State the blood parasite species.
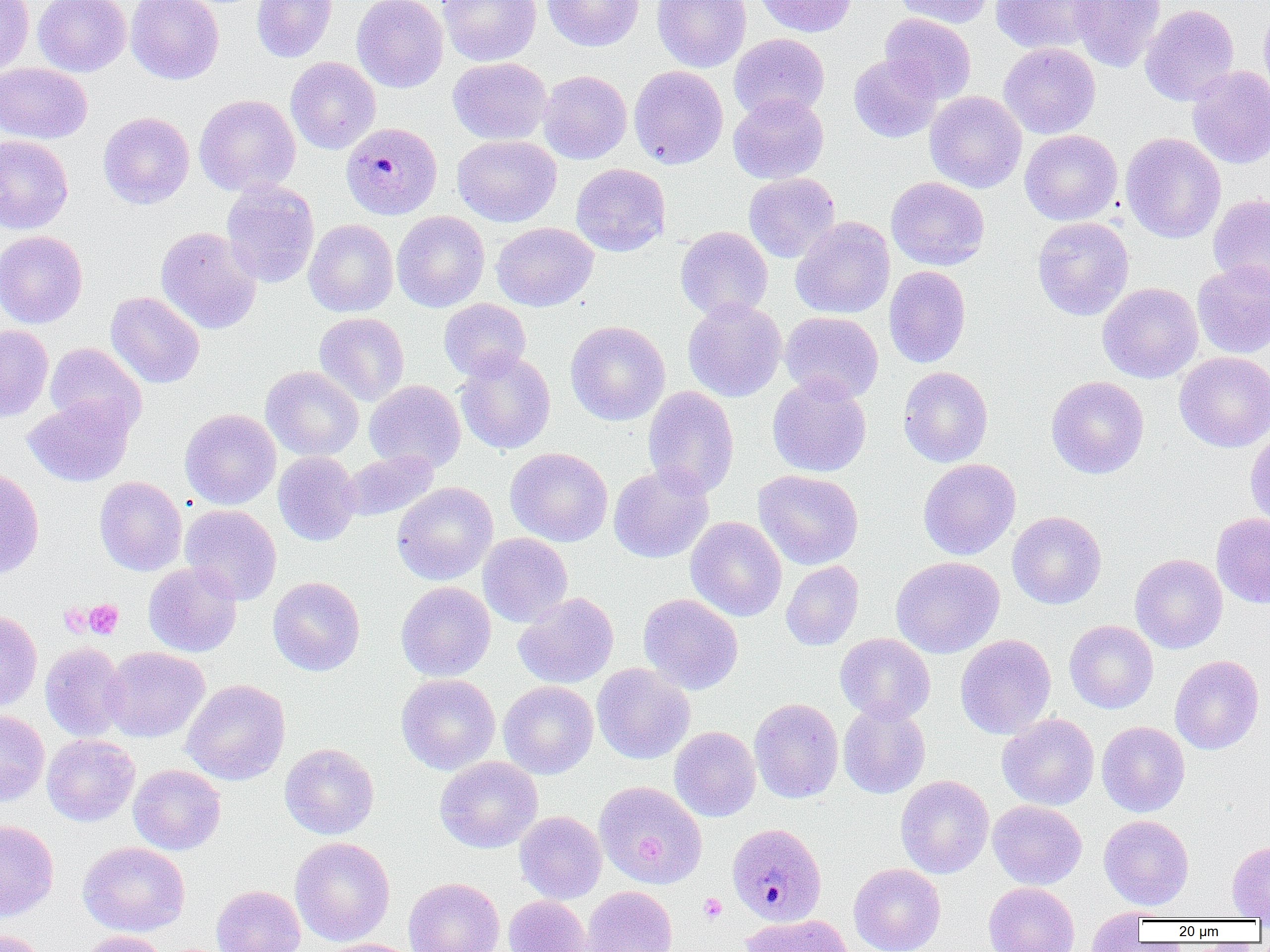

Plasmodium malariae.

preparation = thin blood film
magnification = 1000x
field of view = one of a larger specimen
image size = 1270×952 pixels
modality = optical microscopy
platelet locations = approximate bounding boxes as [x1, y1, x2, y2] in pixels: [83, 599, 123, 639], [698, 894, 727, 922]
Plasmodium malariae-infected red blood cell locations = approximate bounding boxes as [x1, y1, x2, y2] in pixels: [340, 122, 443, 219], [726, 822, 827, 926]
uninfected red blood cell locations = approximate bounding boxes as [x1, y1, x2, y2] in pixels: [0, 0, 34, 76], [34, 0, 131, 76], [126, 0, 224, 84], [251, 0, 337, 62], [351, 0, 448, 92], [438, 0, 542, 66], [542, 0, 644, 51], [652, 0, 751, 72], [754, 0, 857, 37], [892, 0, 995, 28], [990, 0, 1102, 54], [1069, 0, 1167, 72], [1140, 4, 1239, 106], [1259, 5, 1270, 103], [879, 13, 977, 103], [729, 33, 829, 121], [998, 42, 1101, 139], [849, 54, 943, 143], [285, 56, 381, 155], [448, 57, 551, 145], [0, 62, 92, 144], [629, 65, 728, 169], [1187, 66, 1270, 169], [538, 70, 632, 164], [924, 91, 1027, 193], [728, 93, 828, 184], [194, 94, 300, 196], [98, 111, 194, 209], [1019, 130, 1122, 225], [1120, 132, 1226, 243], [0, 135, 73, 234], [452, 135, 561, 227], [570, 163, 671, 257], [743, 172, 840, 263], [886, 176, 990, 270], [221, 180, 319, 287], [1208, 193, 1270, 293], [392, 211, 490, 312], [791, 217, 895, 319], [1032, 217, 1134, 321], [304, 219, 398, 317], [491, 222, 598, 311], [155, 226, 262, 335], [675, 226, 773, 322], [0, 230, 88, 328], [1192, 261, 1270, 359], [883, 265, 971, 368], [1097, 282, 1203, 383], [106, 291, 205, 389], [682, 297, 787, 402], [439, 298, 532, 381], [780, 311, 883, 403], [314, 312, 409, 405], [565, 321, 670, 425], [0, 325, 53, 421], [44, 343, 146, 436], [455, 349, 556, 455], [1174, 351, 1270, 452], [261, 366, 364, 461], [898, 366, 994, 467], [767, 375, 872, 477], [1046, 376, 1149, 479], [364, 380, 466, 473], [643, 386, 739, 498], [23, 395, 135, 487], [180, 409, 281, 509], [1245, 430, 1270, 528], [505, 447, 613, 546], [341, 449, 439, 522], [273, 452, 361, 546], [918, 458, 1021, 560], [608, 463, 714, 563], [0, 467, 44, 579], [753, 469, 863, 569], [94, 476, 187, 576], [392, 482, 498, 585], [180, 504, 282, 604], [1007, 511, 1107, 609], [1211, 512, 1270, 608], [686, 517, 787, 621], [478, 533, 573, 627], [1130, 553, 1227, 653], [891, 556, 1004, 658], [781, 561, 864, 651], [143, 562, 242, 657], [267, 576, 365, 676], [396, 581, 496, 681], [513, 592, 619, 688], [638, 593, 743, 694], [0, 609, 42, 712], [1064, 620, 1159, 714], [835, 633, 935, 724], [955, 634, 1056, 739], [40, 642, 129, 741], [103, 646, 209, 742], [1170, 655, 1264, 754], [592, 663, 695, 764], [396, 673, 500, 774], [182, 679, 291, 785], [498, 680, 598, 779], [749, 698, 843, 803], [838, 702, 930, 799], [0, 709, 49, 806], [997, 713, 1099, 810], [1097, 721, 1190, 817], [669, 726, 760, 822], [42, 734, 140, 826], [280, 743, 379, 839], [435, 756, 543, 853], [128, 764, 226, 855], [895, 775, 994, 878], [594, 781, 707, 889], [988, 800, 1087, 889], [514, 811, 606, 904], [1099, 815, 1194, 910], [0, 819, 59, 921], [290, 837, 395, 946], [78, 841, 190, 936], [1226, 841, 1270, 920], [848, 863, 946, 952], [403, 877, 504, 952], [983, 881, 1079, 952], [211, 884, 306, 952], [582, 886, 677, 952], [504, 896, 591, 952], [1086, 909, 1148, 951], [740, 913, 853, 952], [0, 926, 50, 952], [78, 930, 169, 952], [317, 938, 420, 952]